Identify the cell.
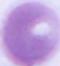

This is an erythrocyte.

modality = micrograph
magnification = 1000x